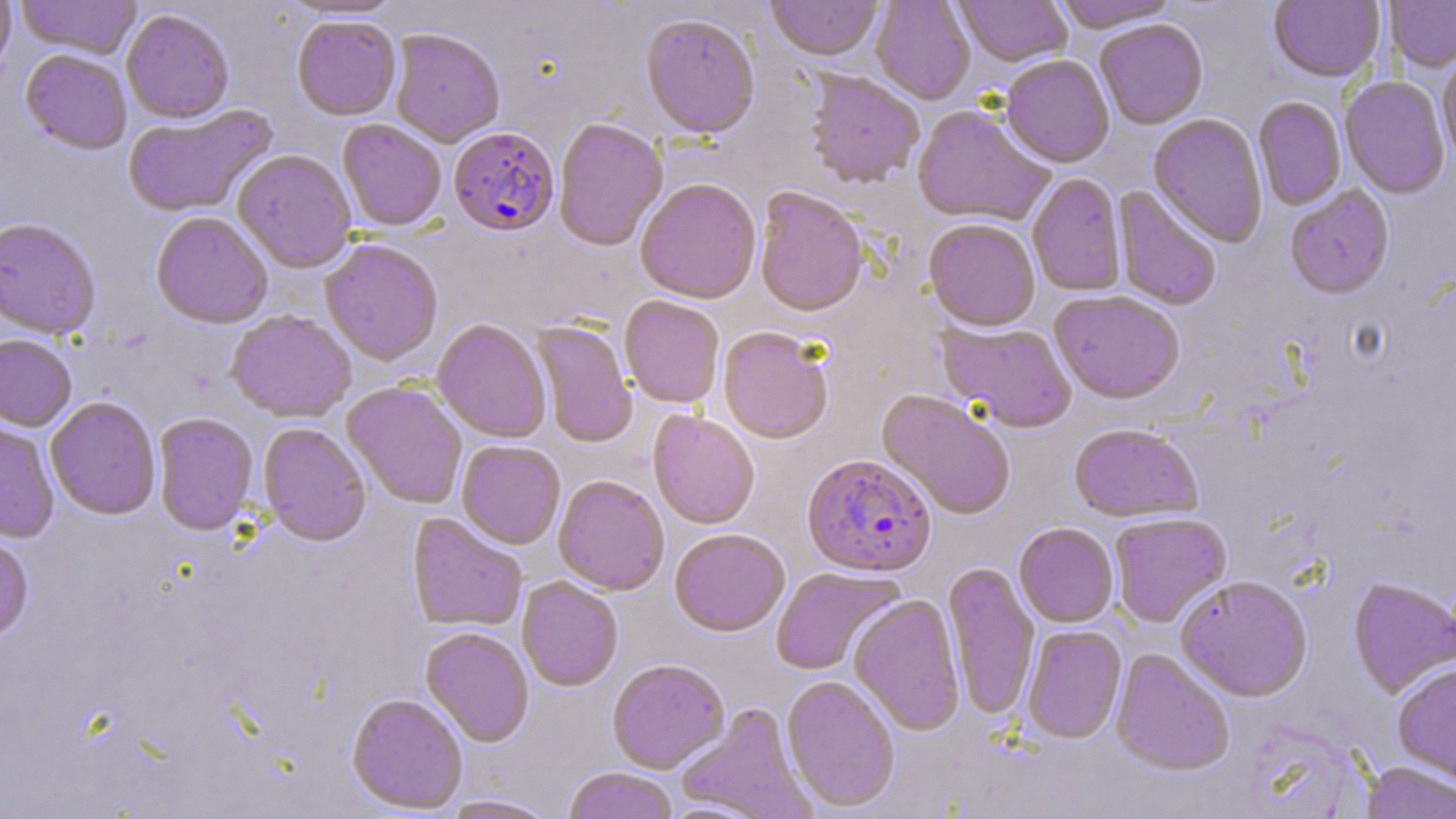

slide-level diagnosis = Plasmodium falciparum
magnification = 1000x
stain = May-Grünwald-Giemsa
uninfected red blood cell locations = approximate bounding boxes as named x1/y1/x2/y2 corners in pixels: (x1=0, y1=0, x2=16, y2=78), (x1=15, y1=0, x2=142, y2=60), (x1=276, y1=0, x2=406, y2=20), (x1=766, y1=0, x2=884, y2=64), (x1=870, y1=0, x2=975, y2=106), (x1=954, y1=0, x2=1072, y2=69), (x1=1052, y1=0, x2=1181, y2=36), (x1=1385, y1=0, x2=1456, y2=75), (x1=1268, y1=1, x2=1385, y2=85), (x1=121, y1=10, x2=234, y2=126), (x1=641, y1=17, x2=759, y2=143), (x1=292, y1=18, x2=400, y2=122), (x1=1095, y1=21, x2=1209, y2=131), (x1=389, y1=31, x2=505, y2=149), (x1=20, y1=51, x2=131, y2=157), (x1=1438, y1=54, x2=1456, y2=169), (x1=1000, y1=56, x2=1115, y2=170), (x1=803, y1=71, x2=924, y2=191), (x1=1339, y1=77, x2=1450, y2=201), (x1=1253, y1=98, x2=1346, y2=212), (x1=123, y1=105, x2=278, y2=219), (x1=912, y1=107, x2=1055, y2=229), (x1=1148, y1=114, x2=1267, y2=249), (x1=553, y1=119, x2=668, y2=254), (x1=337, y1=120, x2=446, y2=233), (x1=233, y1=151, x2=357, y2=274), (x1=1027, y1=175, x2=1127, y2=297), (x1=635, y1=181, x2=761, y2=306), (x1=1112, y1=186, x2=1221, y2=312), (x1=1285, y1=187, x2=1395, y2=301), (x1=753, y1=188, x2=869, y2=320), (x1=151, y1=214, x2=272, y2=331), (x1=0, y1=220, x2=101, y2=342), (x1=923, y1=221, x2=1040, y2=334), (x1=320, y1=241, x2=443, y2=368), (x1=1049, y1=292, x2=1185, y2=407), (x1=619, y1=297, x2=724, y2=410), (x1=226, y1=311, x2=356, y2=424), (x1=432, y1=321, x2=551, y2=443), (x1=937, y1=321, x2=1077, y2=435), (x1=530, y1=322, x2=637, y2=449), (x1=718, y1=330, x2=833, y2=446), (x1=0, y1=336, x2=76, y2=433), (x1=342, y1=383, x2=467, y2=510), (x1=875, y1=390, x2=1015, y2=521), (x1=46, y1=398, x2=160, y2=521), (x1=647, y1=411, x2=759, y2=531), (x1=153, y1=414, x2=258, y2=537), (x1=0, y1=418, x2=59, y2=544), (x1=258, y1=424, x2=371, y2=548), (x1=1068, y1=426, x2=1203, y2=525), (x1=457, y1=442, x2=565, y2=550), (x1=553, y1=477, x2=669, y2=597), (x1=407, y1=514, x2=526, y2=632), (x1=1110, y1=514, x2=1232, y2=629), (x1=1014, y1=524, x2=1118, y2=628), (x1=670, y1=530, x2=789, y2=639), (x1=0, y1=539, x2=34, y2=645), (x1=943, y1=562, x2=1039, y2=721), (x1=770, y1=567, x2=905, y2=677), (x1=517, y1=578, x2=623, y2=692), (x1=1175, y1=578, x2=1313, y2=704), (x1=1348, y1=579, x2=1456, y2=700), (x1=848, y1=596, x2=965, y2=737), (x1=1022, y1=626, x2=1127, y2=745), (x1=420, y1=628, x2=534, y2=748), (x1=1110, y1=649, x2=1235, y2=778), (x1=607, y1=660, x2=729, y2=775), (x1=1393, y1=665, x2=1456, y2=789), (x1=781, y1=676, x2=900, y2=814), (x1=346, y1=695, x2=468, y2=815), (x1=677, y1=704, x2=816, y2=819), (x1=1360, y1=761, x2=1456, y2=819), (x1=563, y1=769, x2=677, y2=819), (x1=438, y1=796, x2=561, y2=819)
field of view = single
image size = 1456×819 pixels
modality = light microscopy
Plasmodium falciparum-infected red blood cell locations = approximate bounding boxes as named x1/y1/x2/y2 corners in pixels: (x1=449, y1=130, x2=560, y2=240), (x1=802, y1=456, x2=937, y2=580)
preparation = thin blood film